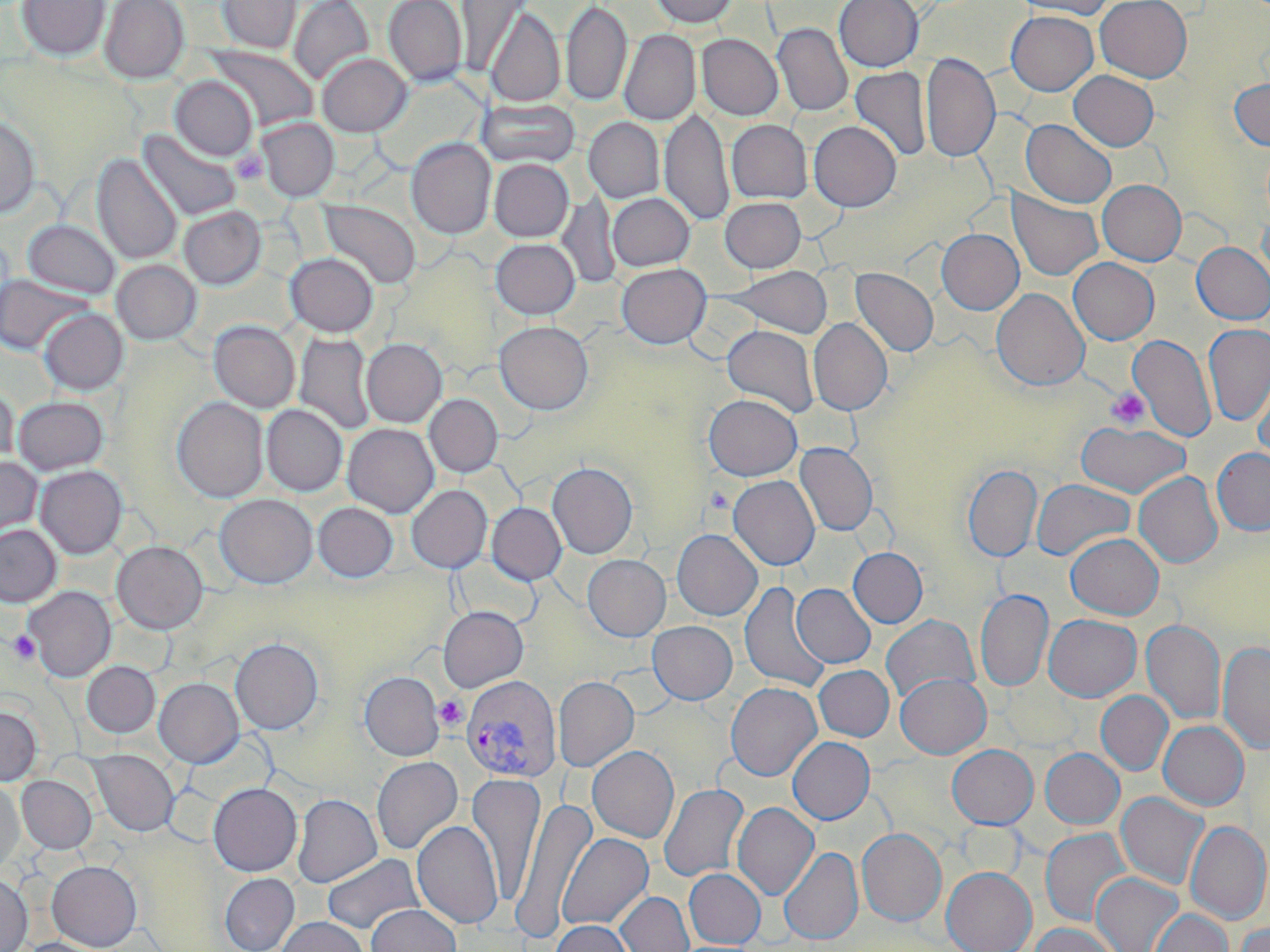

Summary:
  - Coordinate format: approximate bounding boxes as named x1/y1/x2/y2 corners in pixels
  - Platelet locations: (x1=230, y1=149, x2=268, y2=186), (x1=1105, y1=388, x2=1150, y2=429), (x1=706, y1=486, x2=734, y2=515), (x1=8, y1=631, x2=41, y2=664), (x1=434, y1=696, x2=467, y2=729)
  - Uninfected red blood cell locations: (x1=16, y1=0, x2=110, y2=60), (x1=100, y1=0, x2=189, y2=83), (x1=217, y1=0, x2=301, y2=54), (x1=289, y1=0, x2=374, y2=87), (x1=383, y1=0, x2=467, y2=87), (x1=457, y1=0, x2=531, y2=74), (x1=651, y1=0, x2=737, y2=27), (x1=835, y1=0, x2=923, y2=71), (x1=1010, y1=0, x2=1117, y2=19), (x1=1095, y1=0, x2=1192, y2=82), (x1=561, y1=1, x2=632, y2=107), (x1=485, y1=7, x2=565, y2=108), (x1=1006, y1=10, x2=1098, y2=95), (x1=773, y1=23, x2=853, y2=116), (x1=619, y1=30, x2=700, y2=125), (x1=697, y1=34, x2=783, y2=120), (x1=206, y1=45, x2=318, y2=131), (x1=318, y1=53, x2=411, y2=136), (x1=921, y1=53, x2=999, y2=163), (x1=850, y1=65, x2=932, y2=162), (x1=1069, y1=70, x2=1158, y2=150), (x1=170, y1=76, x2=257, y2=160), (x1=1229, y1=78, x2=1270, y2=150), (x1=477, y1=99, x2=580, y2=169), (x1=660, y1=107, x2=733, y2=226), (x1=584, y1=113, x2=732, y2=216), (x1=0, y1=114, x2=40, y2=218), (x1=257, y1=118, x2=339, y2=201), (x1=584, y1=118, x2=664, y2=203), (x1=1021, y1=119, x2=1116, y2=208), (x1=727, y1=120, x2=812, y2=203), (x1=808, y1=121, x2=901, y2=212), (x1=139, y1=130, x2=241, y2=222), (x1=406, y1=138, x2=496, y2=239), (x1=92, y1=153, x2=182, y2=265), (x1=489, y1=159, x2=573, y2=241), (x1=1097, y1=180, x2=1186, y2=266), (x1=1007, y1=191, x2=1102, y2=281), (x1=556, y1=193, x2=622, y2=289), (x1=607, y1=193, x2=695, y2=271), (x1=720, y1=197, x2=806, y2=272), (x1=319, y1=201, x2=420, y2=290), (x1=178, y1=206, x2=266, y2=290), (x1=1257, y1=213, x2=1270, y2=288), (x1=23, y1=220, x2=120, y2=299), (x1=936, y1=229, x2=1024, y2=315), (x1=491, y1=238, x2=580, y2=319), (x1=1192, y1=242, x2=1270, y2=324), (x1=285, y1=253, x2=378, y2=336), (x1=1068, y1=257, x2=1159, y2=345), (x1=112, y1=260, x2=201, y2=345), (x1=616, y1=263, x2=711, y2=348), (x1=722, y1=266, x2=834, y2=338), (x1=851, y1=268, x2=938, y2=357), (x1=0, y1=274, x2=91, y2=356), (x1=991, y1=288, x2=1089, y2=391), (x1=39, y1=308, x2=128, y2=395), (x1=809, y1=318, x2=892, y2=415), (x1=209, y1=321, x2=300, y2=412), (x1=494, y1=321, x2=593, y2=414), (x1=1202, y1=324, x2=1270, y2=426), (x1=722, y1=325, x2=819, y2=416), (x1=295, y1=333, x2=376, y2=435), (x1=1128, y1=334, x2=1216, y2=443), (x1=362, y1=338, x2=447, y2=427), (x1=1253, y1=364, x2=1270, y2=465), (x1=0, y1=385, x2=19, y2=469), (x1=424, y1=394, x2=503, y2=476), (x1=704, y1=394, x2=802, y2=480), (x1=13, y1=396, x2=108, y2=475), (x1=172, y1=397, x2=268, y2=502), (x1=262, y1=405, x2=347, y2=495), (x1=262, y1=414, x2=440, y2=499), (x1=1075, y1=421, x2=1190, y2=499), (x1=343, y1=423, x2=439, y2=517), (x1=795, y1=442, x2=878, y2=536), (x1=1212, y1=448, x2=1270, y2=536), (x1=0, y1=456, x2=43, y2=541), (x1=547, y1=461, x2=638, y2=558), (x1=963, y1=464, x2=1042, y2=562), (x1=35, y1=465, x2=127, y2=558), (x1=1133, y1=472, x2=1222, y2=568), (x1=728, y1=475, x2=820, y2=570), (x1=1031, y1=479, x2=1135, y2=561), (x1=407, y1=485, x2=492, y2=572), (x1=215, y1=494, x2=318, y2=588), (x1=313, y1=502, x2=398, y2=582), (x1=487, y1=502, x2=566, y2=585), (x1=0, y1=524, x2=61, y2=607), (x1=672, y1=529, x2=762, y2=620), (x1=1066, y1=533, x2=1164, y2=620), (x1=112, y1=540, x2=208, y2=633), (x1=847, y1=547, x2=927, y2=627), (x1=583, y1=554, x2=670, y2=641), (x1=739, y1=582, x2=830, y2=693), (x1=792, y1=584, x2=875, y2=667), (x1=803, y1=585, x2=882, y2=742), (x1=23, y1=586, x2=115, y2=681), (x1=975, y1=589, x2=1053, y2=692), (x1=439, y1=606, x2=528, y2=691), (x1=1043, y1=614, x2=1141, y2=701), (x1=880, y1=615, x2=980, y2=705), (x1=1142, y1=620, x2=1225, y2=724), (x1=647, y1=621, x2=737, y2=704), (x1=230, y1=637, x2=323, y2=734), (x1=1218, y1=642, x2=1270, y2=754), (x1=82, y1=661, x2=160, y2=738), (x1=814, y1=665, x2=894, y2=741), (x1=360, y1=672, x2=444, y2=761), (x1=895, y1=673, x2=990, y2=758), (x1=553, y1=676, x2=638, y2=771), (x1=154, y1=678, x2=244, y2=767), (x1=726, y1=682, x2=821, y2=781), (x1=1096, y1=691, x2=1173, y2=775), (x1=0, y1=704, x2=41, y2=786), (x1=1158, y1=721, x2=1249, y2=810), (x1=788, y1=737, x2=874, y2=824), (x1=947, y1=744, x2=1037, y2=828), (x1=587, y1=746, x2=679, y2=843), (x1=1041, y1=748, x2=1124, y2=828), (x1=89, y1=750, x2=179, y2=836), (x1=372, y1=756, x2=462, y2=855), (x1=466, y1=773, x2=544, y2=904), (x1=17, y1=775, x2=96, y2=853), (x1=0, y1=779, x2=23, y2=872), (x1=208, y1=783, x2=301, y2=876), (x1=658, y1=783, x2=749, y2=883), (x1=1116, y1=792, x2=1208, y2=890), (x1=292, y1=794, x2=381, y2=887), (x1=513, y1=795, x2=597, y2=940), (x1=732, y1=802, x2=818, y2=899), (x1=412, y1=820, x2=503, y2=928), (x1=1186, y1=822, x2=1269, y2=924), (x1=857, y1=828, x2=946, y2=926), (x1=1041, y1=828, x2=1130, y2=927), (x1=557, y1=832, x2=652, y2=931), (x1=779, y1=847, x2=862, y2=944), (x1=322, y1=854, x2=424, y2=935), (x1=47, y1=860, x2=142, y2=950), (x1=942, y1=867, x2=1035, y2=952), (x1=684, y1=868, x2=766, y2=948), (x1=0, y1=873, x2=32, y2=952), (x1=220, y1=873, x2=299, y2=952), (x1=1092, y1=873, x2=1182, y2=952), (x1=616, y1=891, x2=694, y2=952), (x1=366, y1=904, x2=460, y2=952), (x1=1150, y1=909, x2=1232, y2=952), (x1=276, y1=917, x2=369, y2=952), (x1=551, y1=920, x2=634, y2=952), (x1=1234, y1=922, x2=1270, y2=952), (x1=1028, y1=923, x2=1120, y2=952), (x1=20, y1=938, x2=108, y2=952)
  - Plasmodium vivax-infected red blood cell locations: (x1=462, y1=675, x2=561, y2=783)
  - Slide-level diagnosis: Plasmodium vivax
  - Image size: 1270×952 pixels
  - Preparation: thin blood film
  - Stain: May-Grünwald-Giemsa
  - Field of view: one of a larger specimen
  - Magnification: 1000x
  - Modality: optical microscopy